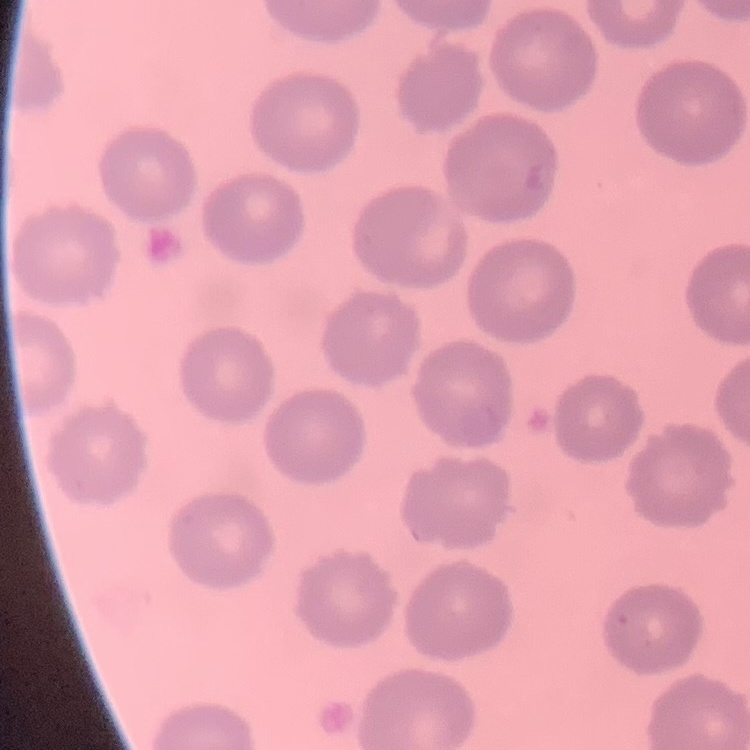

erythrocyte morphology = no rouleaux formation
stain = Field's or Giemsa
image type = one tile cut from a larger photomicrograph
preparation = thin blood smear